State which parasite is depicted.
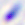

This is Toxoplasma gondii.

modality: photomicrograph
magnification: 400x